Look for parasitized red blood cells.
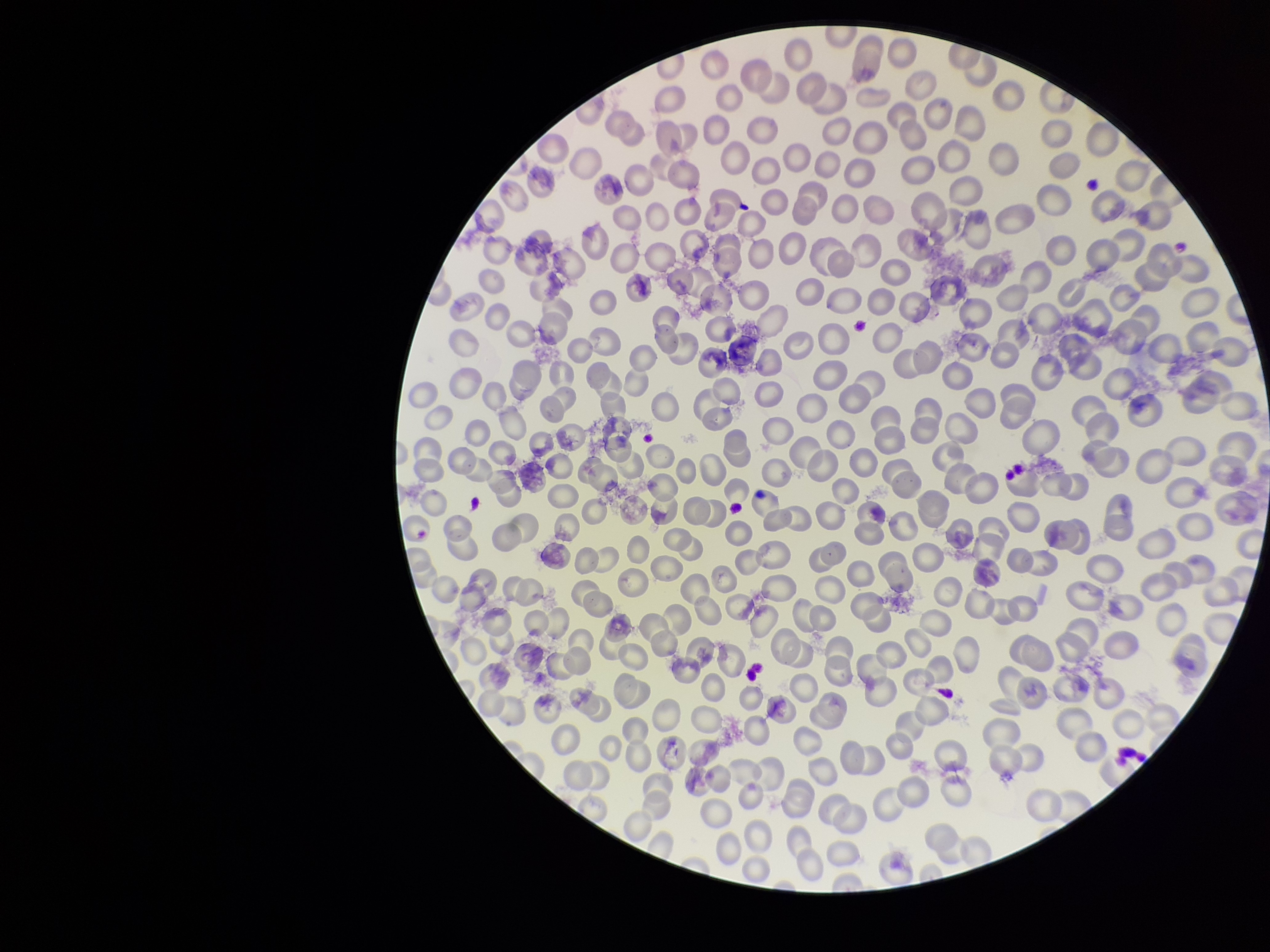

None seen.

Stained with Giemsa. Photographed through the microscope eyepiece with a smartphone camera. One field from this slide. Image is 1270×952 pixels. Preparation: thin smear. Parasitized red blood cell count: 0. Patient malaria status: negative. Red blood cell count: 276.